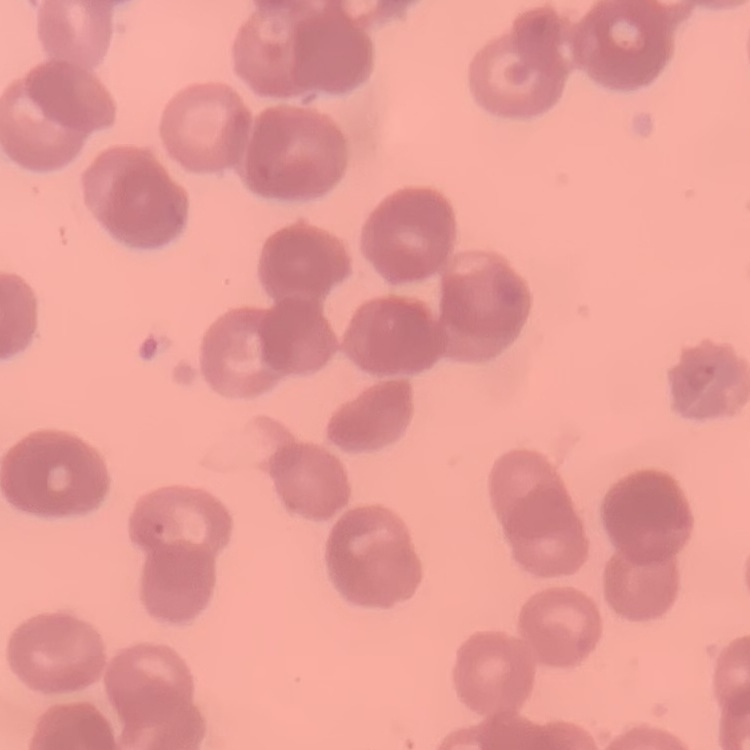

The red blood cells exhibit rouleaux formation. One tile cut from a larger photomicrograph. Stained with either Field's or Giemsa. Thin peripheral smear.